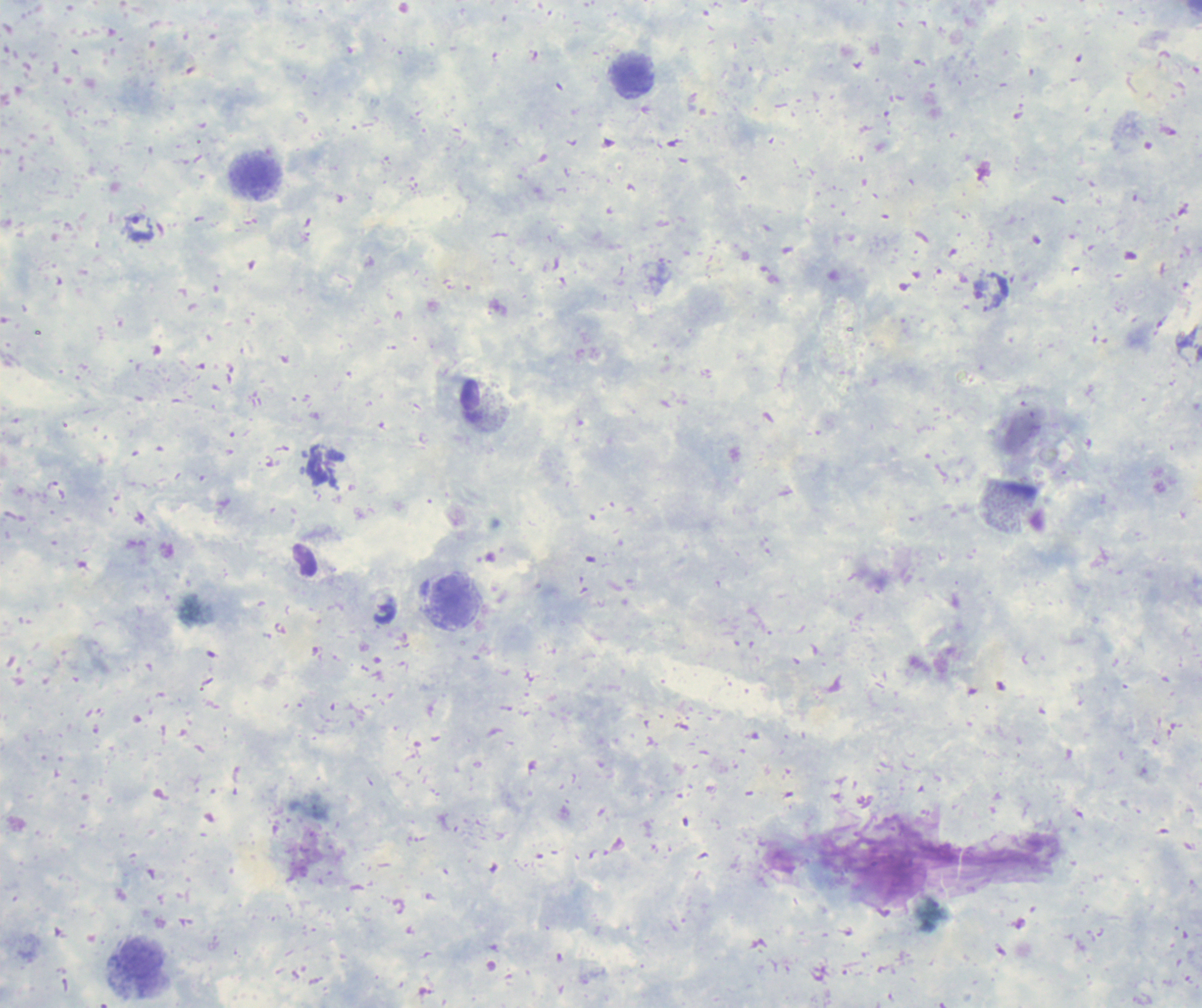
Approximate object centers, in pixels from the top-left corner.
Summary:
  - Leukocyte locations: (x=637, y=79), (x=255, y=177), (x=454, y=602), (x=141, y=969)
  - Trophozoite locations: (x=140, y=229)
  - Image size: 1202×1008 pixels
  - Result: malaria parasites detected
  - Background quality: unsatisfactory
  - Preparation: thick smear of blood
  - Context: previously used in an actual diagnosis
  - Stain: Romanowsky
  - Field of view: one from this slide
  - Magnification: 100x